State which cell type is depicted.
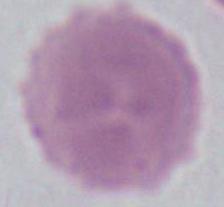
An erythrocyte.

{
  "magnification": "1000x",
  "modality": "photomicrograph"
}